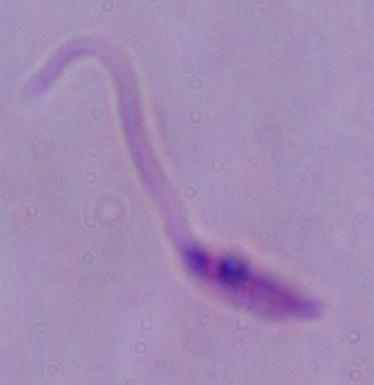
A Leishmania parasite is seen. 1000x magnification. Photomicrograph.